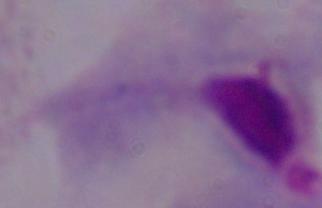
identification = trichomonad
modality = micrograph
magnification = 1000x